State which cell type is depicted.
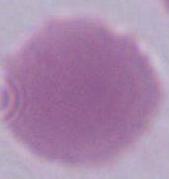
An erythrocyte.

1000x magnification. Micrograph.